Assess the morphology of the red blood cells.
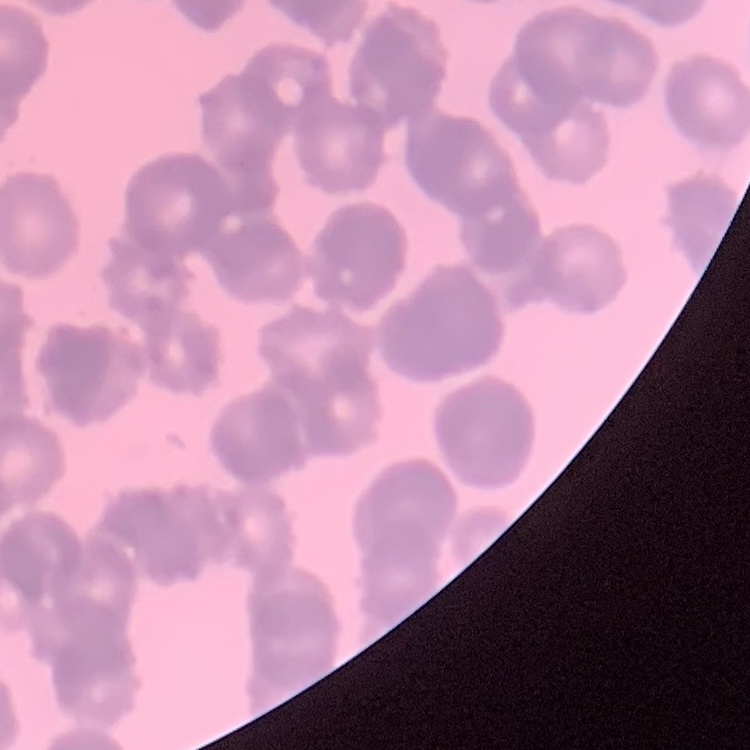
Rouleaux formation.

Summary:
  - Image type: one tile cut from a larger photomicrograph
  - Stain: Field's or Giemsa
  - Preparation: thin blood smear